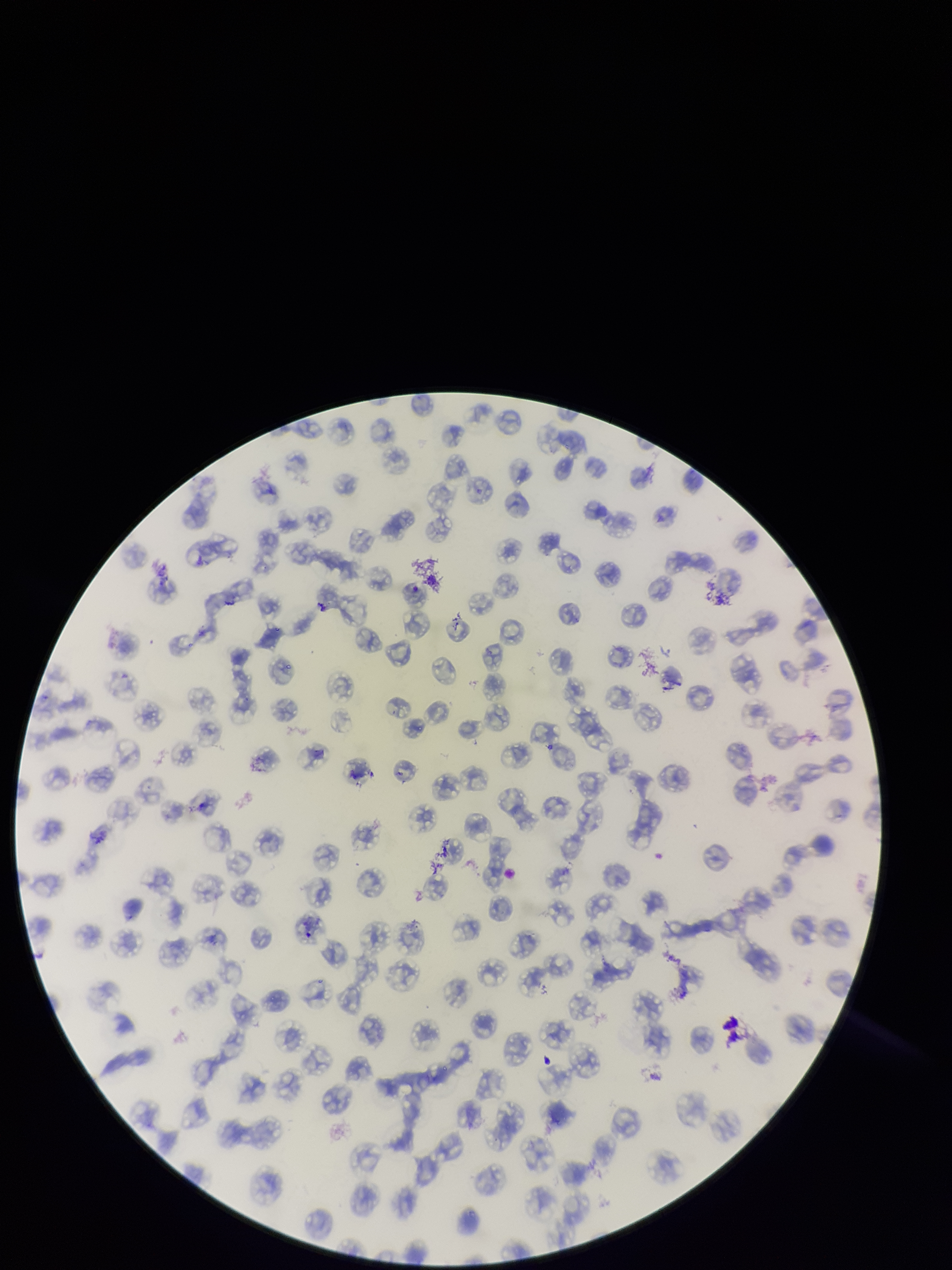
Parasitized red blood cell count: 0. One field from this slide. Giemsa stain. Species reported for this patient: Plasmodium falciparum. Image is 952×1270 pixels. Preparation: thin smear. Photographed through the microscope eyepiece with a smartphone camera. Red blood cell count: 169. Patient malaria status: infected. Parasitized red blood cells: none detected.